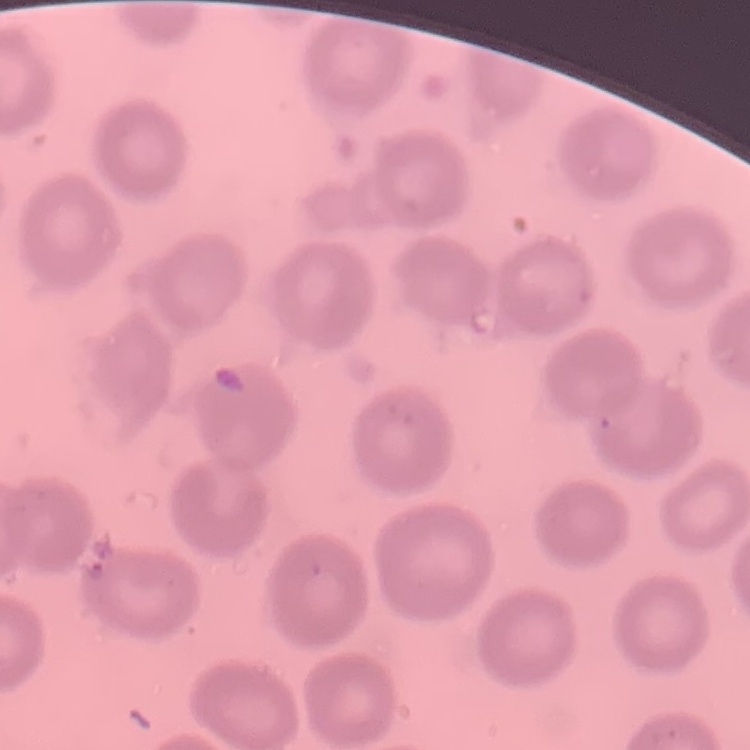

Summary:
  - Red blood cell morphology: no rouleaux formation
  - Preparation: thin blood smear
  - Image type: one tile cut from a larger photomicrograph
  - Stain: Field's or Giemsa